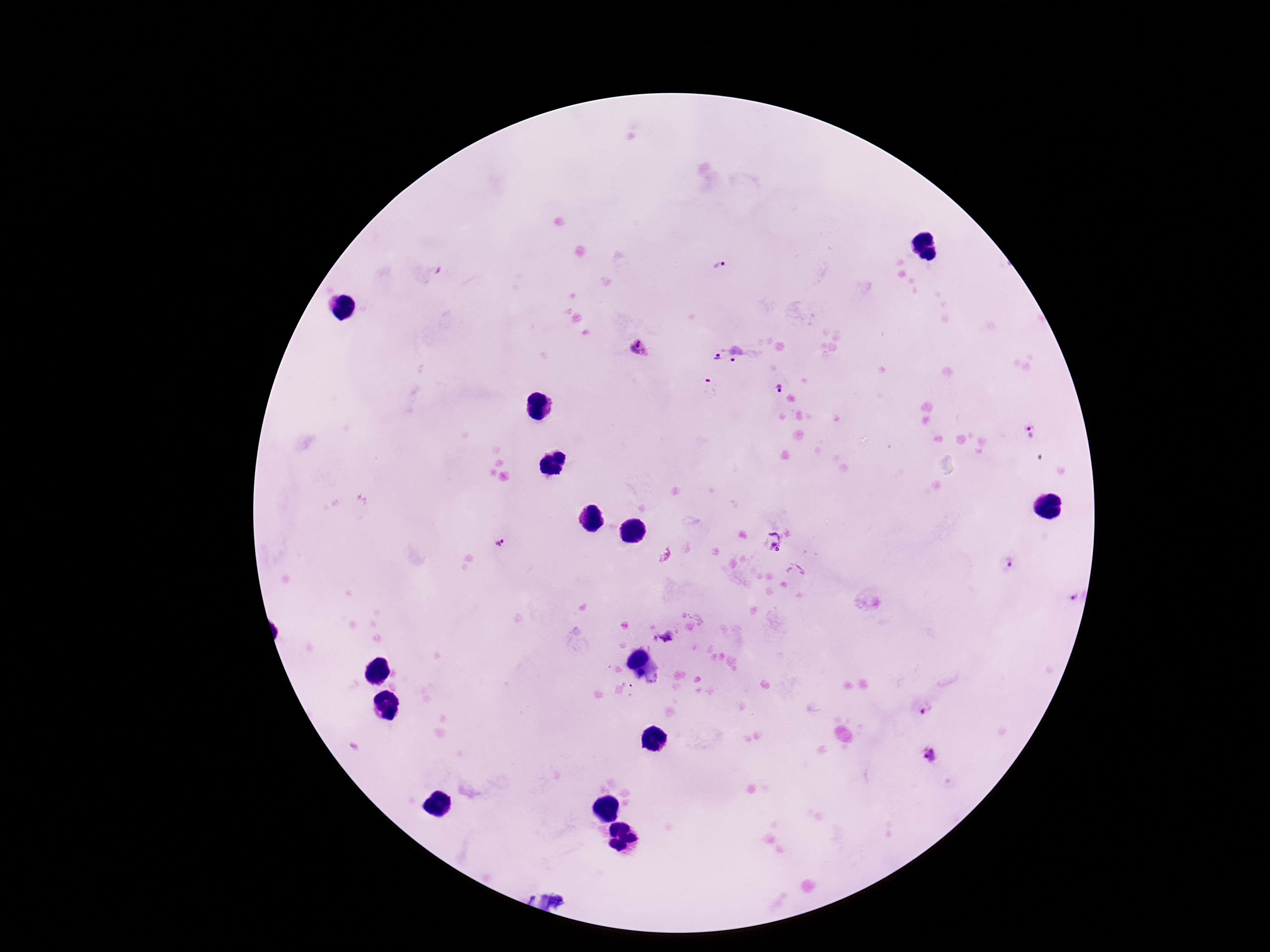

Approximate object centers, in pixels from the top-left corner. Plasmodium parasite locations: (x=720, y=266), (x=637, y=348), (x=739, y=353), (x=717, y=357), (x=708, y=385), (x=779, y=388), (x=1026, y=430), (x=772, y=539), (x=499, y=544), (x=1008, y=564), (x=1076, y=598), (x=667, y=638), (x=924, y=708), (x=930, y=754). Giemsa stain. 100x magnification. Photographed through the microscope eyepiece with a smartphone camera. Image is 1270×952 pixels. One field from this slide. Thick peripheral-blood smear. Patient malaria status: infected.